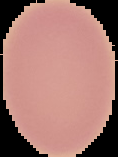
result = no Plasmodium parasites seen
image size = 118×157 pixels
image type = segmented cell region on a black background
preparation = thin blood smear